Assess the morphology of the erythrocytes.
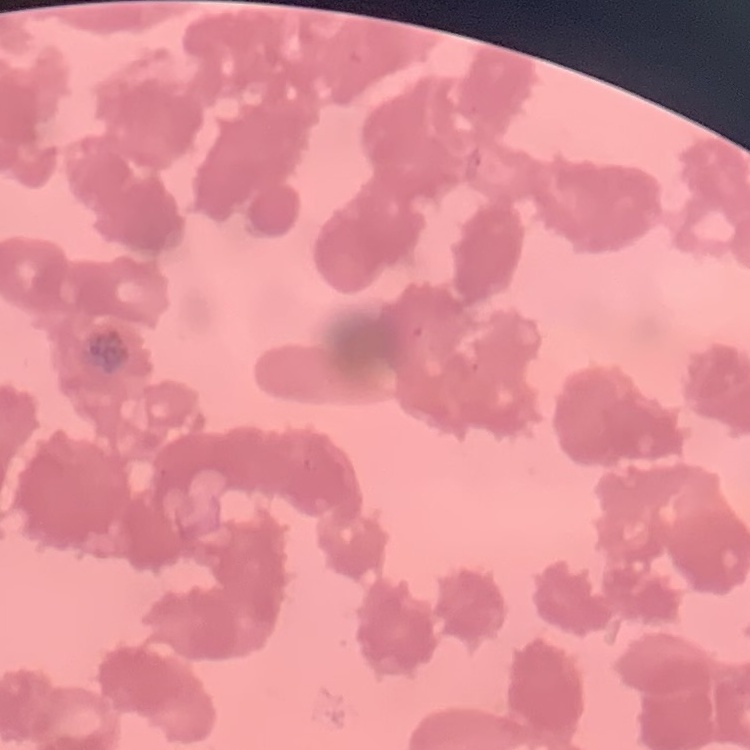
They show rouleaux formation.

Square crop of a larger photomicrograph. Field's or Giemsa stain. Thin blood film.